Point out every malaria parasite.
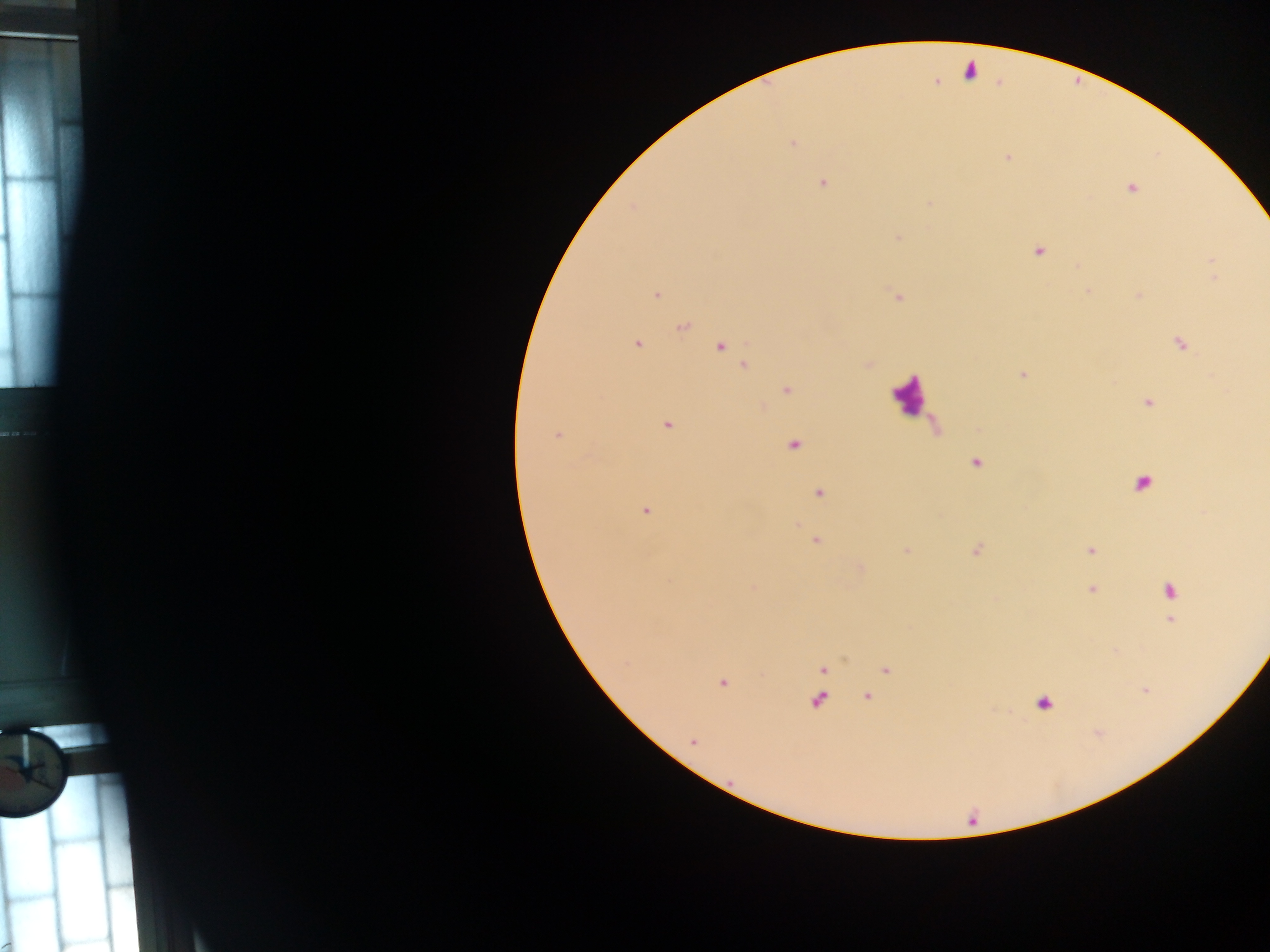

Approximate centers as {x, y} in pixels.
Malaria parasites: {970, 71}, {793, 143}, {1008, 157}, {823, 184}, {1130, 188}, {899, 238}, {1038, 251}, {656, 294}, {1138, 295}, {899, 297}, {683, 326}, {636, 344}, {1180, 344}, {720, 346}, {745, 366}, {1023, 374}, {787, 390}, {1148, 402}, {667, 426}, {556, 436}, {794, 445}, {976, 463}, {1143, 482}, {819, 493}, {646, 510}, {816, 541}, {1090, 550}, {1091, 589}, {1169, 590}, {1172, 621}, {823, 669}, {885, 670}, {723, 683}, {868, 696}, {818, 701}, {1044, 704}, {693, 741}.

country = Ghana
field of view = single
capture = mobile-phone photograph through a microscope
image size = 1270×952 pixels
leukocyte locations = approximate centers as {x, y} in pixels: {911, 395}
preparation = thick blood smear